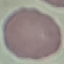
Summary:
  - Malaria status: uninfected
  - Preparation: thin blood film
  - Stain: Giemsa
  - Capture: smartphone camera at the microscope eyepiece
  - Image type: automatically extracted cell patch, resized to 64 × 64 pixels